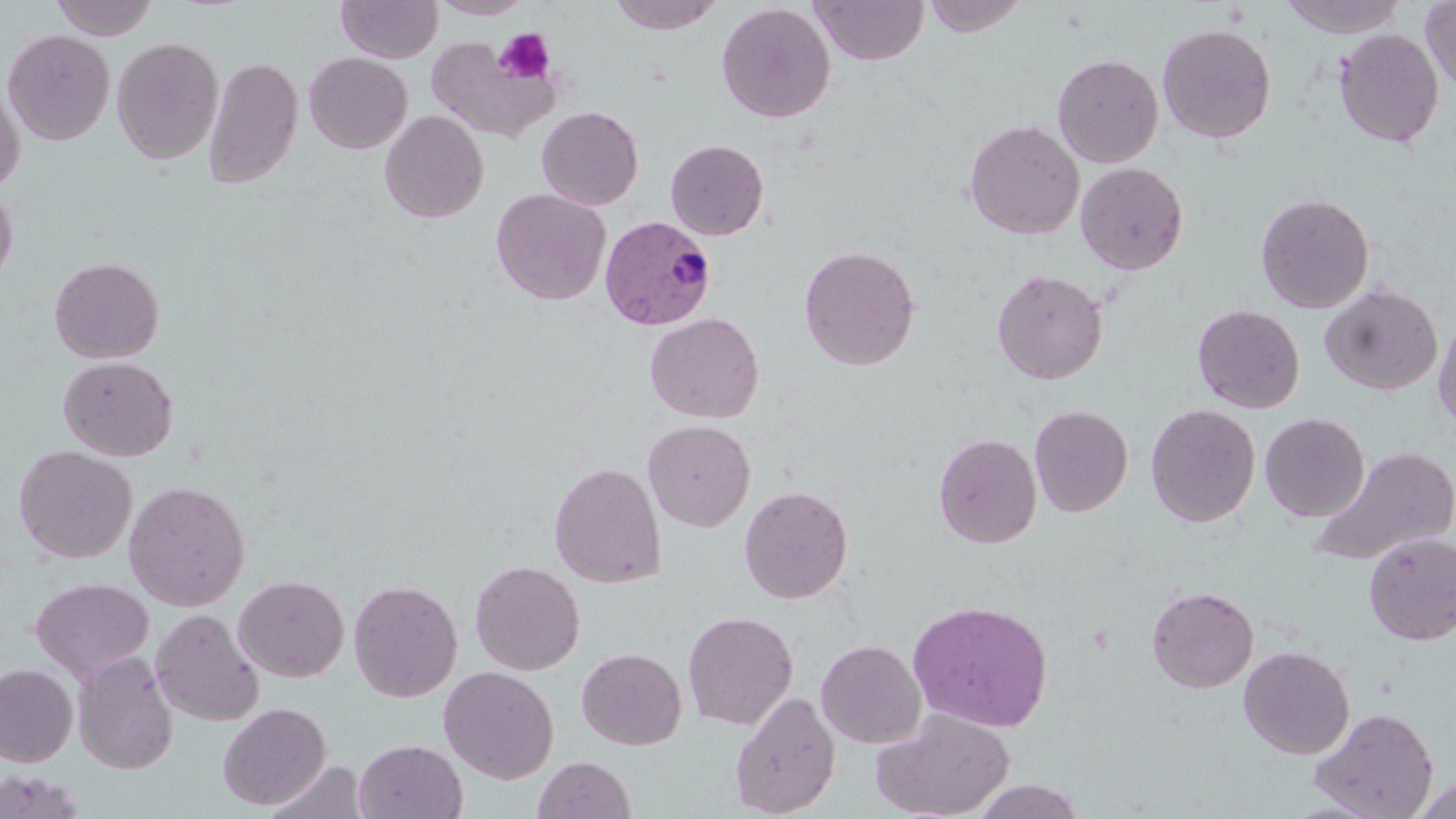

slide_level_diagnosis: Plasmodium vivax
modality: light microscopy
image_size: 1456×819 pixels
field_of_view: one of a larger specimen
platelet_locations: 'approximate bounding boxes as (x1,y1)-(x2,y2) corner pairs in pixels: (494,28)-(555,84)'
stain: May-Grünwald-Giemsa
preparation: thin blood smear
magnification: 1000x
plasmodium_vivax_infected_red_blood_cell_locations: 'approximate bounding boxes as (x1,y1)-(x2,y2) corner pairs in pixels: (600,215)-(718,331)'
uninfected_red_blood_cell_locations: 'approximate bounding boxes as (x1,y1)-(x2,y2) corner pairs in pixels: (49,0)-(160,40), (336,0)-(443,63), (429,0)-(533,19), (608,0)-(724,34), (811,0)-(929,65), (922,0)-(1029,37), (1278,0)-(1409,37), (1420,0)-(1455,93), (716,3)-(836,123), (1157,22)-(1276,143), (2,28)-(115,146), (1334,28)-(1443,147), (111,36)-(223,165), (425,36)-(560,143), (304,52)-(412,153), (1052,53)-(1164,168), (203,56)-(303,188), (0,79)-(25,193), (536,105)-(644,210), (380,109)-(488,223), (964,119)-(1085,239), (665,139)-(769,240), (1076,162)-(1189,274), (0,184)-(18,290), (491,188)-(610,305), (1256,192)-(1375,313), (799,245)-(921,370), (49,256)-(164,363), (992,269)-(1108,384), (1320,283)-(1443,396), (1192,303)-(1305,413), (644,312)-(765,423), (1433,312)-(1456,432), (57,355)-(178,461), (1145,403)-(1261,527), (1030,405)-(1133,517), (1260,412)-(1370,522), (643,419)-(756,532), (933,432)-(1042,548), (13,444)-(138,564), (1306,445)-(1456,567), (549,461)-(667,588), (122,480)-(251,612), (739,485)-(854,604), (1363,533)-(1456,645), (470,559)-(585,675), (233,574)-(350,682), (30,577)-(155,682), (349,579)-(463,702), (46,582)-(169,760), (1146,585)-(1259,693), (906,599)-(1054,732), (150,608)-(264,726), (683,610)-(798,730), (816,638)-(926,748), (1239,645)-(1355,759), (576,647)-(686,750), (72,651)-(178,774), (0,663)-(78,767), (439,665)-(559,784), (730,690)-(840,817), (217,701)-(332,810), (1309,706)-(1439,819), (870,709)-(1015,818), (354,739)-(468,819), (533,755)-(636,819), (266,761)-(368,818), (0,769)-(86,819), (1409,775)-(1456,818), (968,778)-(1087,818)'